Assess the morphology of the red blood cells.
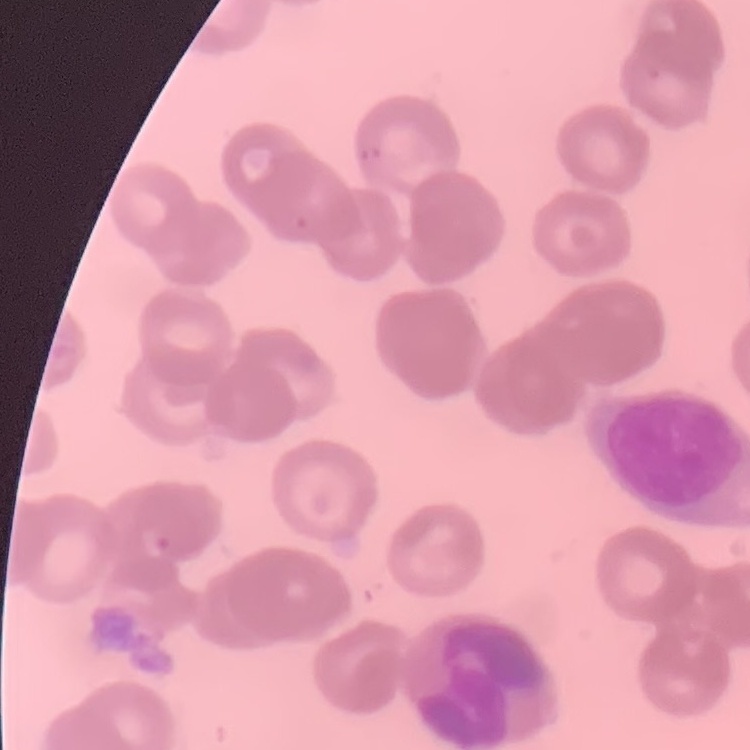
Rouleaux formation.

One tile cut from a larger photomicrograph. Field's or Giemsa stain. Thin blood film.